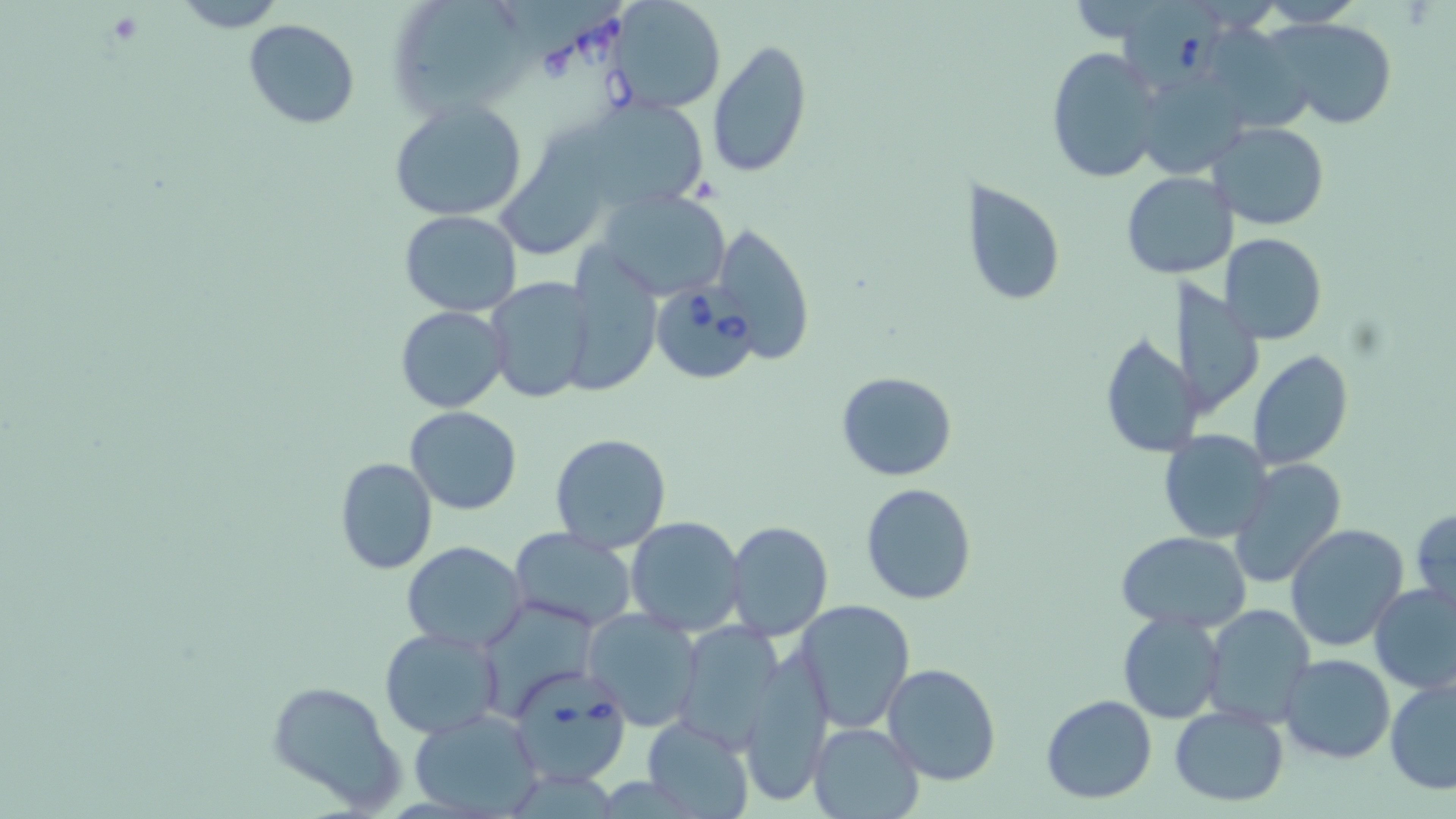
slide-level diagnosis = Babesia divergens
preparation = thin blood film
image size = 1456×819 pixels
magnification = 1000x
modality = light microscopy
field of view = single
Babesia divergens-infected red blood cell locations = approximate bounding boxes as (x1,y1)-(x2,y2) corner pairs in pixels: (1117,0)-(1225,94), (651,283)-(760,385), (506,666)-(633,787)
stain = May-Grünwald-Giemsa
uninfected red blood cell locations = approximate bounding boxes as (x1,y1)-(x2,y2) corner pairs in pixels: (168,0)-(292,31), (388,0)-(534,120), (1258,0)-(1365,27), (612,1)-(725,114), (1267,17)-(1397,131), (243,18)-(361,128), (706,38)-(813,180), (1046,46)-(1165,185), (1137,68)-(1251,181), (389,99)-(529,222), (599,99)-(708,205), (496,121)-(626,263), (1210,122)-(1330,231), (1122,172)-(1232,275), (959,177)-(1065,309), (597,188)-(733,302), (398,210)-(521,315), (709,220)-(814,365), (1221,233)-(1327,343), (561,250)-(660,396), (485,277)-(594,404), (1173,277)-(1262,421), (394,306)-(509,413), (1098,331)-(1198,459), (1249,351)-(1353,470), (835,372)-(958,482), (404,406)-(523,515), (1158,431)-(1273,543), (549,432)-(672,553), (334,456)-(438,576), (1230,458)-(1347,587), (860,483)-(977,605), (1411,508)-(1455,612), (626,516)-(745,637), (725,521)-(833,641), (1284,523)-(1410,653), (509,528)-(637,633), (1117,531)-(1252,632), (401,541)-(528,653), (1370,580)-(1456,695), (795,600)-(915,732), (1200,604)-(1313,727), (583,609)-(703,730), (1118,612)-(1226,725), (673,622)-(786,749), (378,627)-(504,741), (737,651)-(833,806), (1278,654)-(1396,764), (881,663)-(1001,786), (1383,673)-(1456,795), (265,680)-(407,812), (1041,693)-(1158,803), (1169,704)-(1289,805), (410,707)-(546,817), (643,716)-(756,818), (808,721)-(924,819)